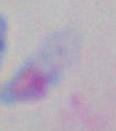

{
  "modality": "micrograph",
  "identification": "Toxoplasma gondii",
  "magnification": "1000x"
}